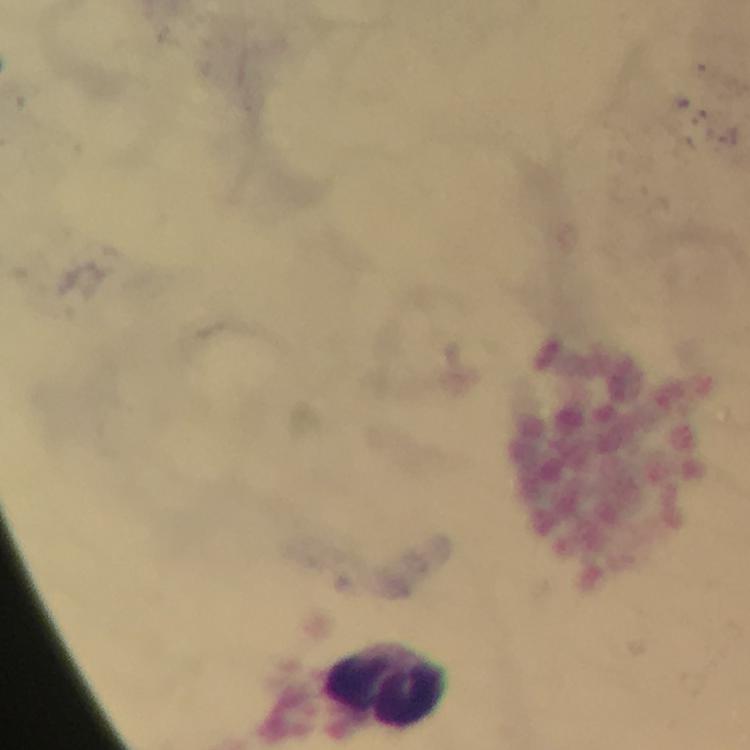
Approximate centers as (x, y) in pixels. Leukocyte locations: (387, 684). From a diagnostic examination for malaria. Plasmodium parasites: none seen. Immersion oil was used. Giemsa stain. Image is 750×750 pixels. Photographed with a smartphone mounted on the microscope. Cropped region of a single field of view. Thick blood smear. At 100x magnification.